Evaluate for malaria.
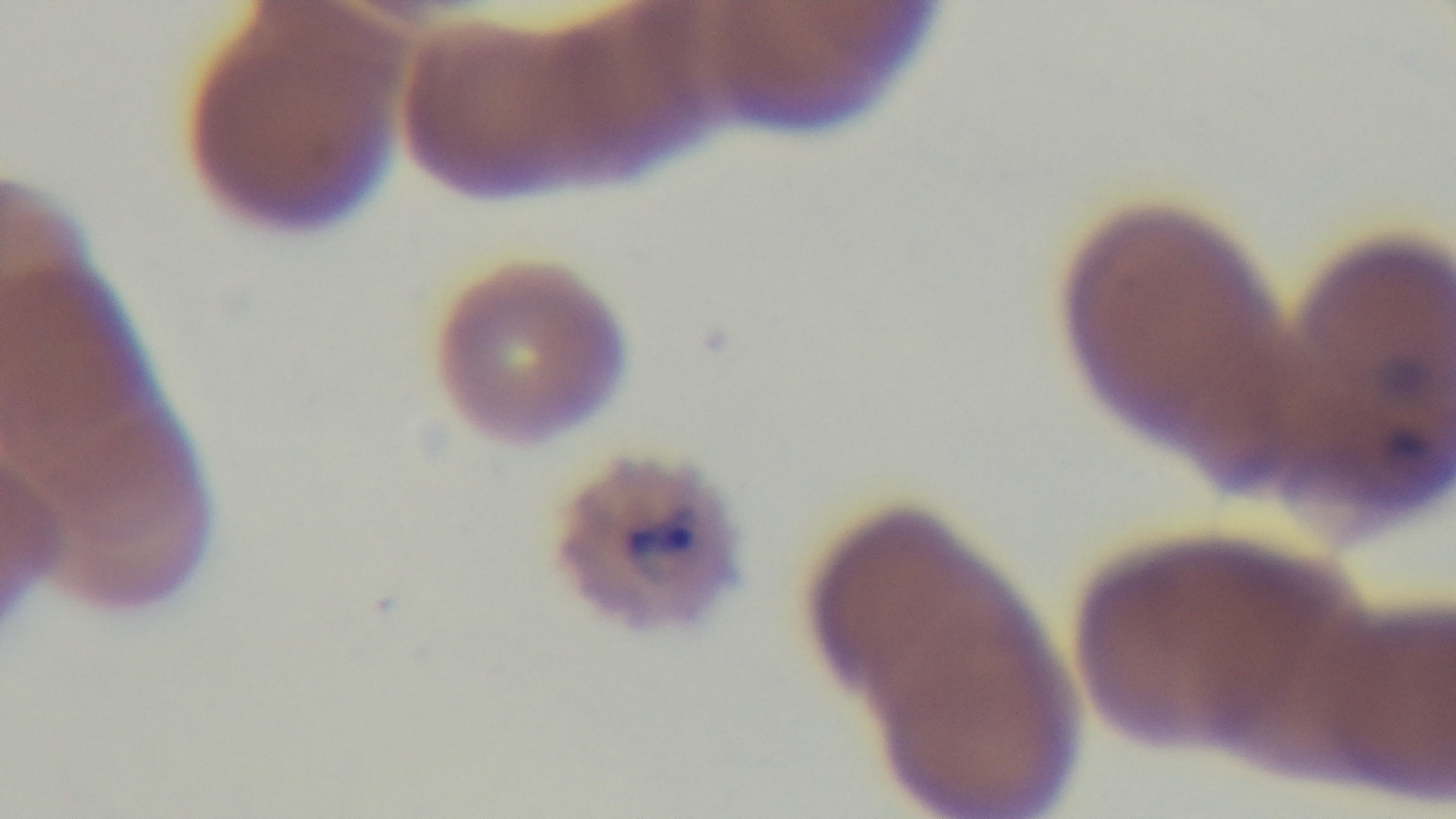

It is infected.

One field from the slide. Giemsa stain. Photomicrograph. Oil-immersion objective, 100x. Preparation: thin. Mounted 4K digital camera.